Classify this cell by malaria status.
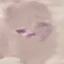

Uninfected.

Summary:
  - Capture: smartphone through the microscope eyepiece
  - Preparation: thin smear
  - Image type: cell patch, automatically extracted from a larger field of view and resized to 64 × 64 pixels
  - Stain: Giemsa